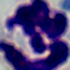

Captured at 1000x magnification. A white blood cell is seen. Micrograph.